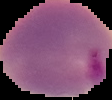 Segmented cell region on a black background. Image is 112×100 pixels. From a thin blood film. Malaria status: parasitized.